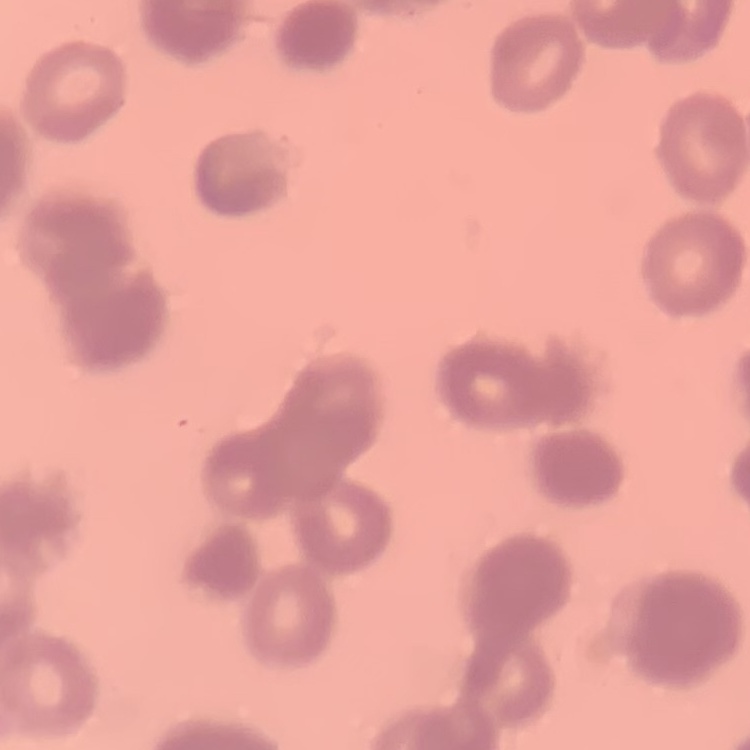

The red blood cells exhibit rouleaux formation. Square crop of a larger photomicrograph. Thin blood film. Stained with either Field's or Giemsa.